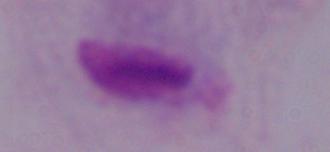

Summary:
  - Modality: micrograph
  - Magnification: 1000x
  - Identification: trichomonad